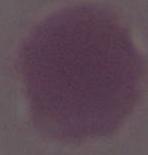 Captured at 1000x magnification. An erythrocyte is shown. Photomicrograph.